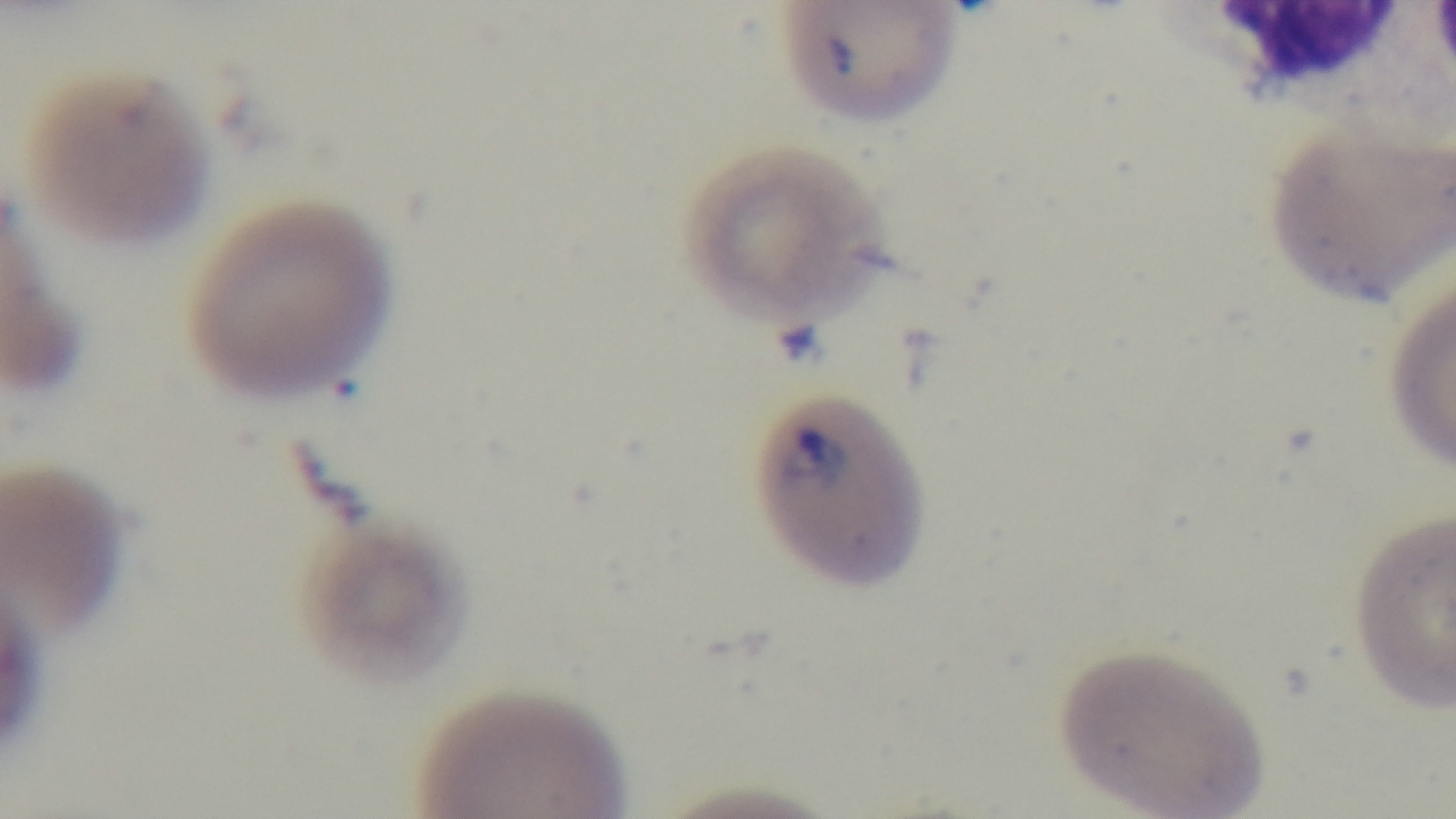
modality = light microscopy
stain = Giemsa
malaria status = positive
capture = mounted 4K digital camera
field of view = single
preparation = thin
objective = 100x oil immersion